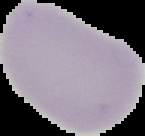

The area outside the segmented cell region is set to black. From a thin blood smear. Image is 145×136 pixels. Result: negative for malaria parasites.